Classify this cell by malaria status.
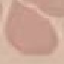

Uninfected.

Summary:
  - Image type: automatically extracted cell patch, resized to 64 × 64 pixels
  - Stain: Giemsa
  - Preparation: thin blood smear
  - Capture: smartphone through the microscope eyepiece